State which parasite is depicted.
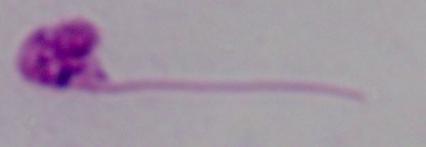

This is Leishmania.

1000x magnification. Micrograph.